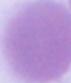
1000x magnification. Micrograph. An erythrocyte is shown.